Assess this cell for malaria.
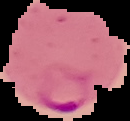
It is parasitized.

Segmented cell region on a black background. Image is 130×121 pixels. From a thin blood smear.